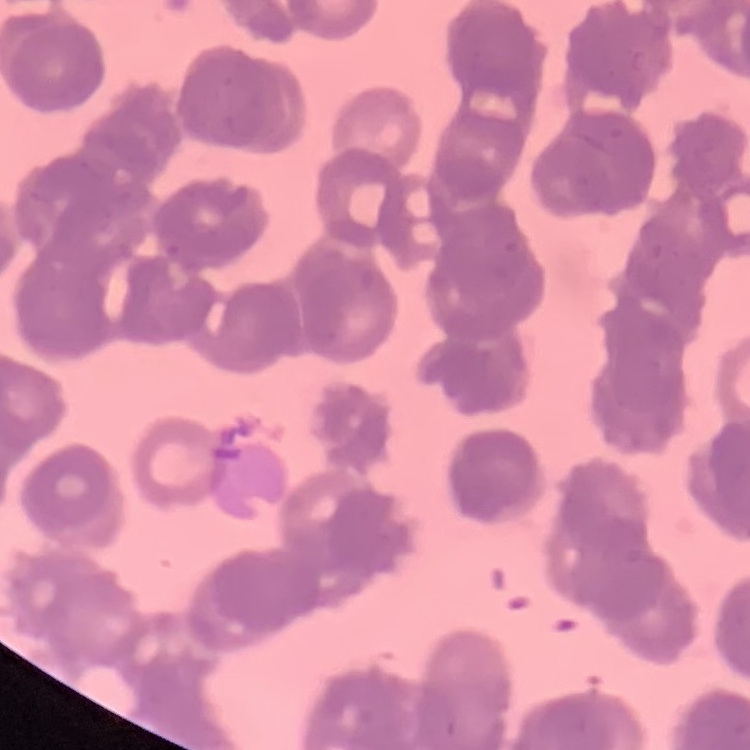

Summary:
  - Red blood cell morphology: rouleaux formation
  - Image type: square crop of a larger photomicrograph
  - Stain: Field's or Giemsa
  - Preparation: thin blood film